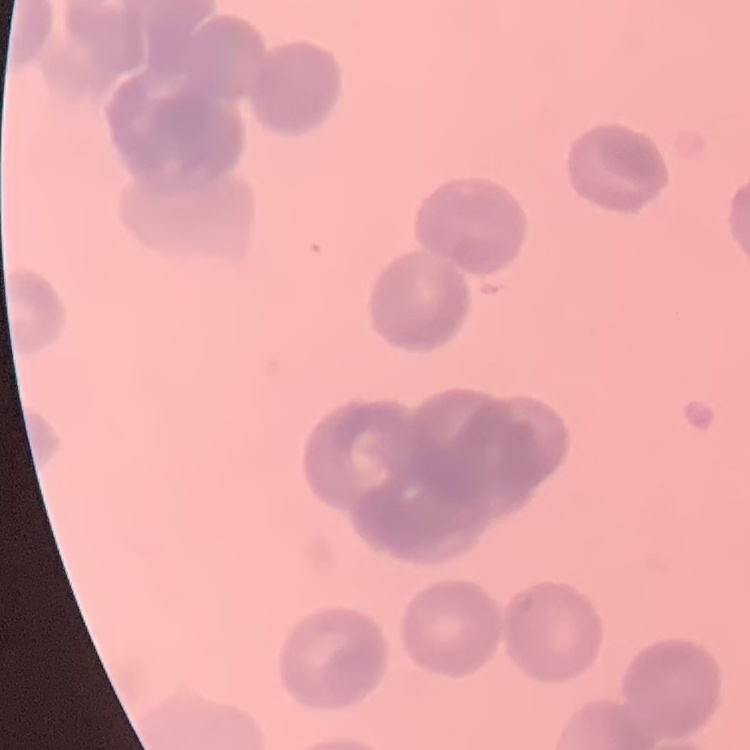

The red blood cells exhibit rouleaux formation. One tile cut from a larger photomicrograph. Thin blood film. Field's or Giemsa stain.